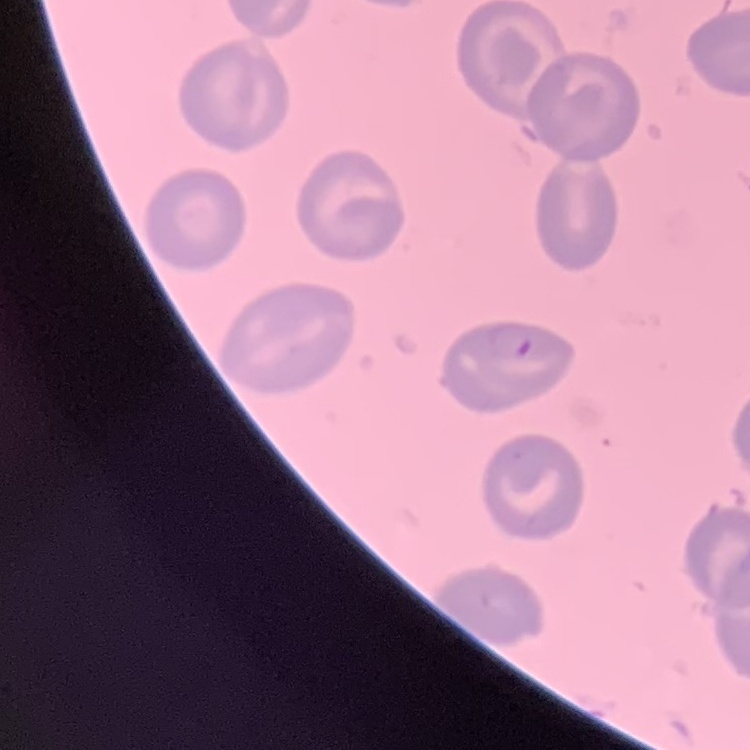 The red blood cells exhibit no rouleaux formation. Thin blood film. Field's or Giemsa stain. Square crop of a larger photomicrograph.